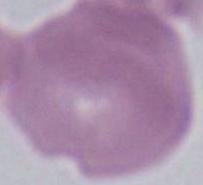
magnification = 1000x
identification = erythrocyte
modality = photomicrograph